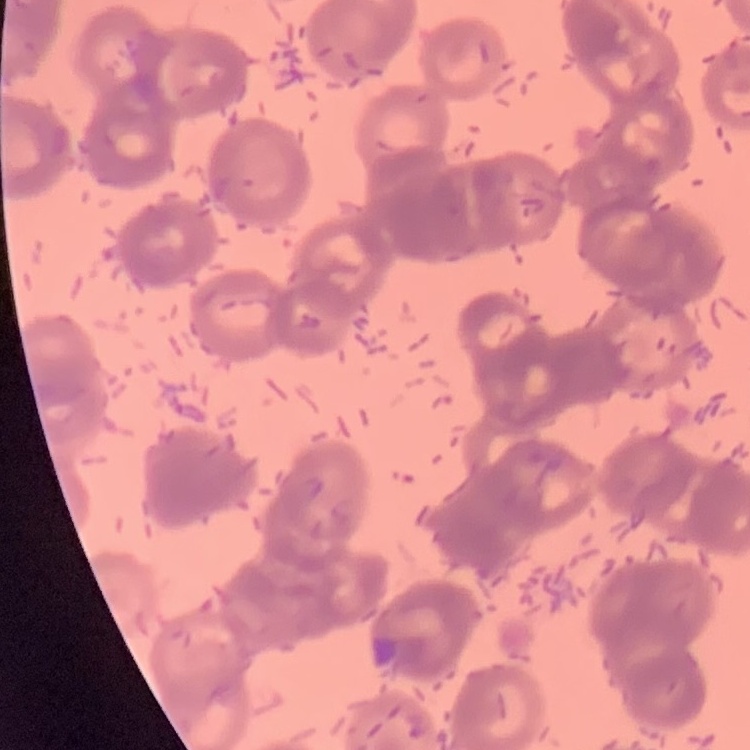
red blood cell morphology = rouleaux formation
stain = Field's or Giemsa
preparation = thin blood film
image type = one tile cut from a larger photomicrograph